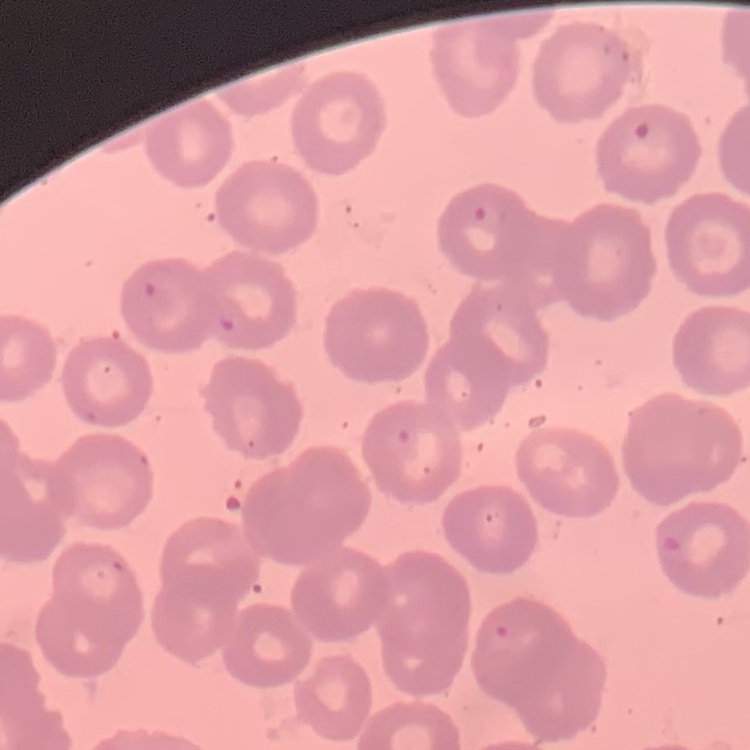

Summary:
  - Red blood cell morphology: no rouleaux formation
  - Image type: one tile cut from a larger photomicrograph
  - Preparation: thin blood film
  - Stain: Field's or Giemsa